Assess this cell for malaria.
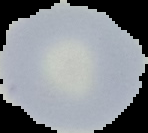
It is uninfected.

Summary:
  - Preparation: thin blood smear
  - Image size: 148×133 pixels
  - Image type: cell region segmented out of the field of view; surrounding area masked to black